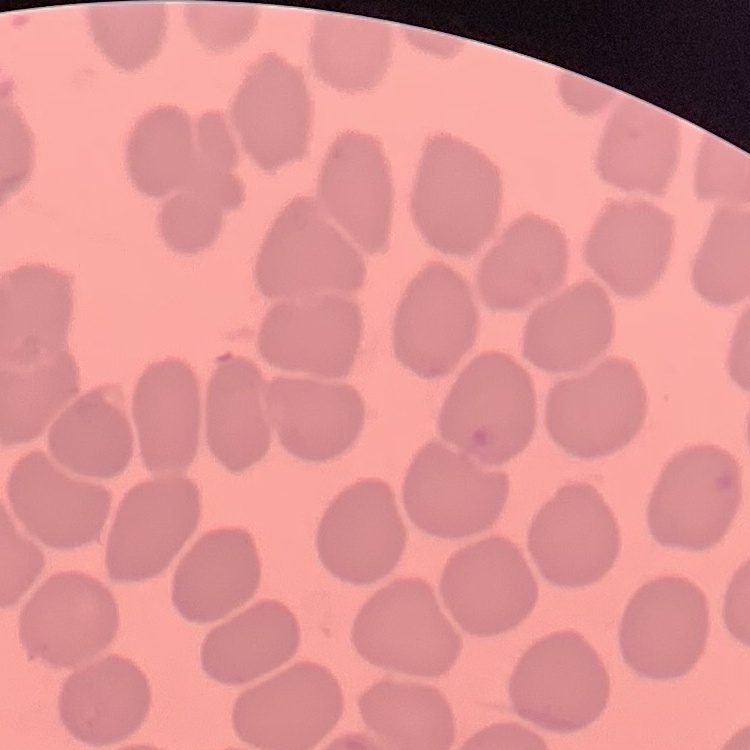

Summary:
  - Erythrocyte morphology: no rouleaux formation
  - Preparation: thin blood film
  - Stain: Field's or Giemsa
  - Image type: square crop of a larger photomicrograph